Identify the parasite.
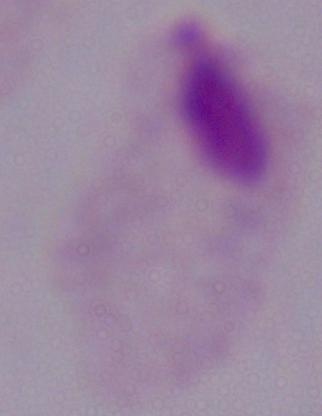
This is a trichomonad.

Summary:
  - Magnification: 1000x
  - Modality: micrograph